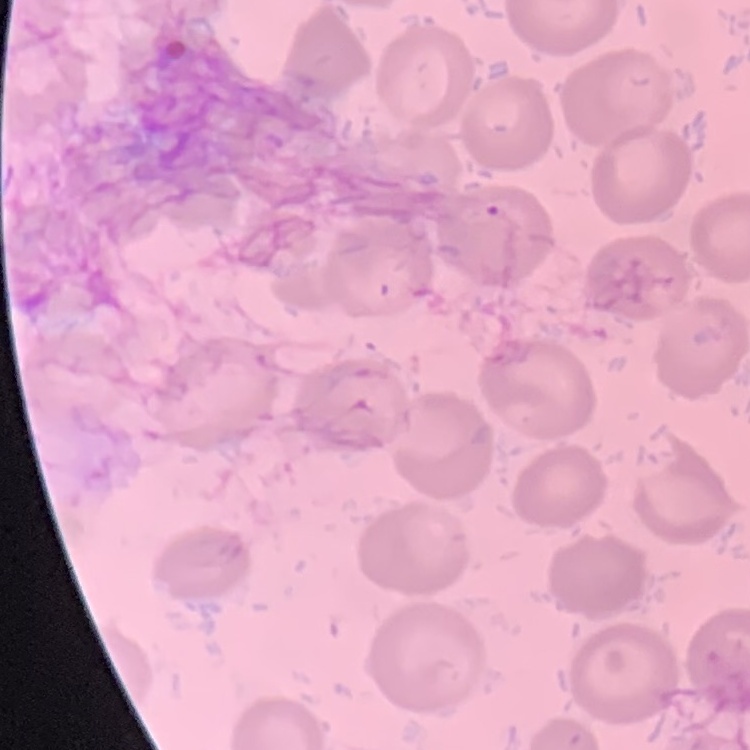
{
  "red_blood_cell_morphology": "no rouleaux formation",
  "stain": "Field's or Giemsa",
  "preparation": "thin blood film",
  "image_type": "one tile cut from a larger photomicrograph"
}